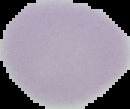

Summary:
  - Malaria status: uninfected
  - Preparation: thin blood film
  - Image type: segmented cell region on a black background
  - Image size: 130×109 pixels